Locate every Plasmodium parasite and every leukocyte.
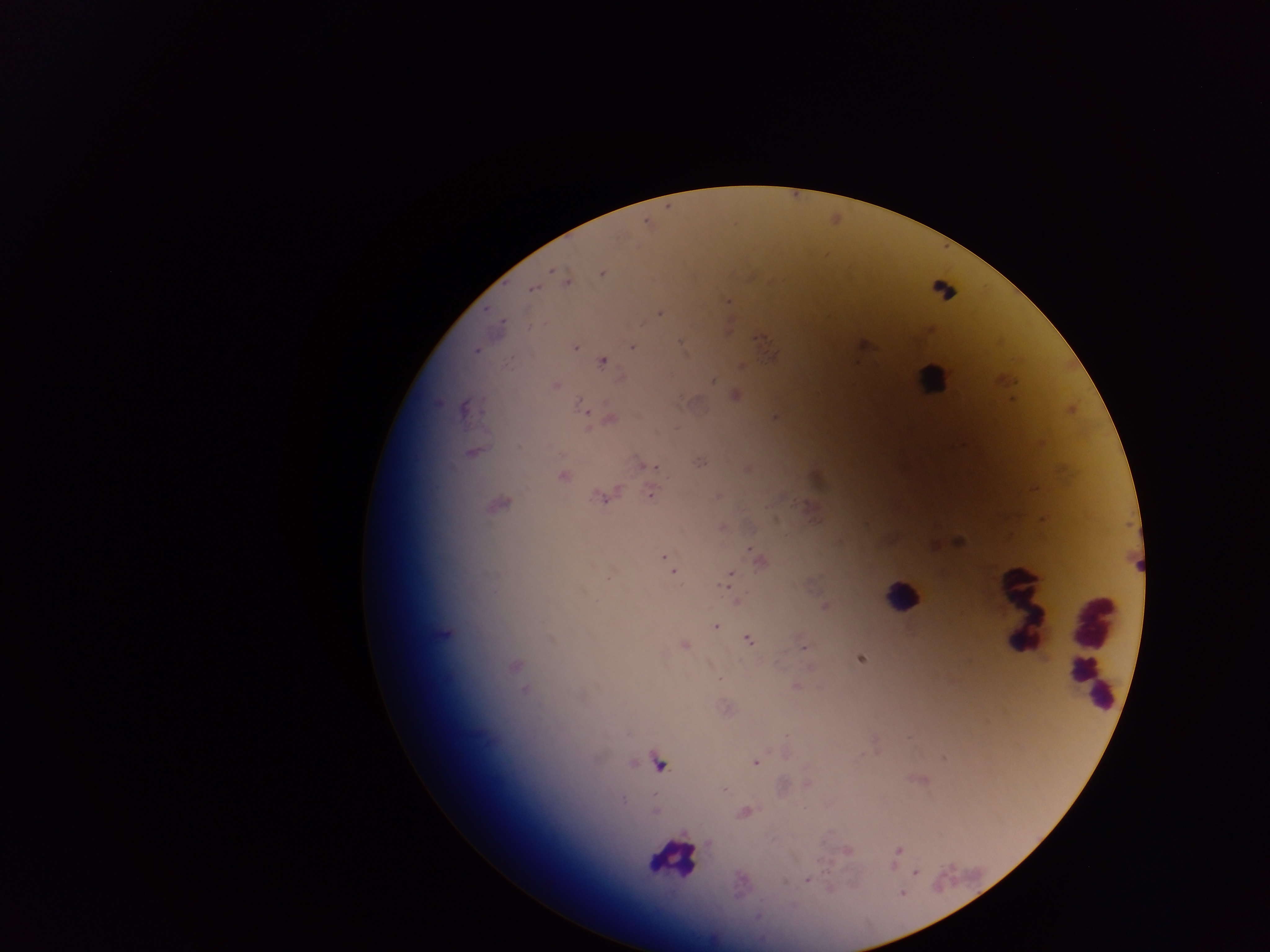

Approximate centers as (x, y) in pixels.
Plasmodium parasites: (551, 271), (602, 273), (566, 281), (533, 288), (728, 301), (659, 313), (681, 342), (865, 346), (575, 347), (633, 347), (476, 351), (772, 356), (602, 362), (742, 365), (713, 381), (556, 385), (735, 396), (582, 407), (464, 408), (775, 417), (609, 420), (471, 452), (700, 462), (649, 466), (563, 476), (650, 495), (603, 498), (957, 541), (667, 559), (759, 560), (672, 570), (729, 577), (737, 600), (825, 606), (716, 626), (749, 640), (684, 645), (804, 648), (860, 658), (515, 666), (720, 679), (796, 686), (525, 690), (944, 757), (755, 763), (659, 764), (807, 785), (724, 790), (623, 800), (655, 811), (744, 813), (899, 849), (848, 850), (915, 873), (808, 880), (785, 881), (829, 890), (902, 893).
Leukocytes: (944, 284), (931, 377), (902, 596), (1022, 609), (1093, 649), (668, 858).

capture: mobile-phone photograph through a microscope
field_of_view: single
country: Ghana
preparation: thick blood smear
image_size: 1270×952 pixels